Give the position of every malaria parasite.
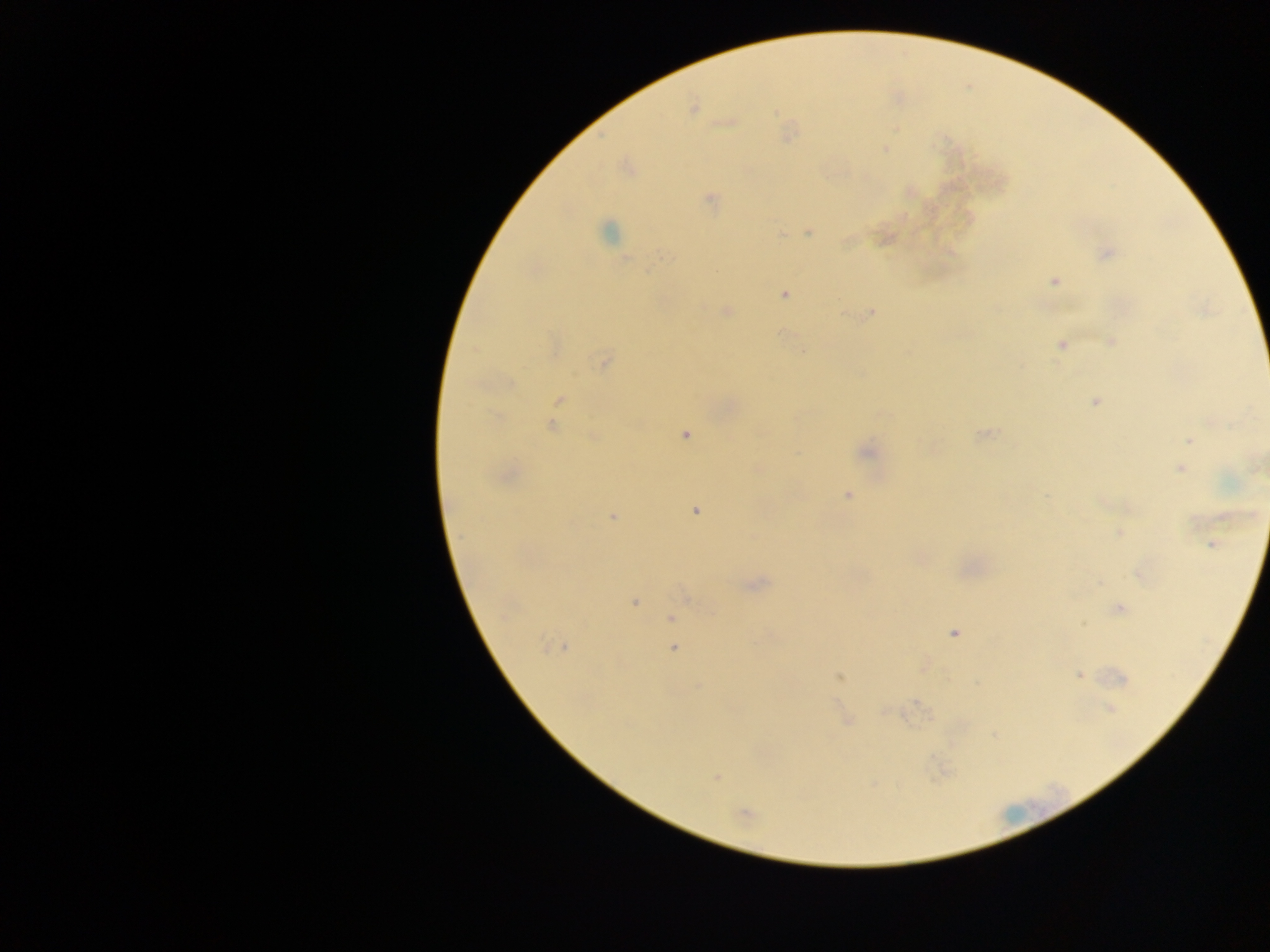
Approximate centers as (x, y) in pixels.
Malaria parasites: (692, 108), (728, 123), (884, 149), (709, 199), (809, 232), (608, 233), (781, 234), (1106, 253), (647, 270), (1055, 281), (784, 294), (726, 311), (871, 312), (1111, 341), (1060, 344), (804, 351), (604, 362), (560, 399), (1095, 402), (552, 426), (685, 435), (985, 435), (593, 436), (1189, 441), (867, 452), (1180, 468), (848, 495), (695, 511), (612, 517), (1119, 533), (1212, 544), (1139, 575), (758, 583), (635, 603), (1119, 609), (671, 618), (954, 634), (556, 646), (674, 648), (1079, 675), (839, 677), (1123, 678), (1110, 708), (847, 721), (716, 778), (745, 814).

Image is 1270×952 pixels. Thick blood film. Collected in Ghana. One field of view. Photographed through a microscope with a mobile-phone camera.